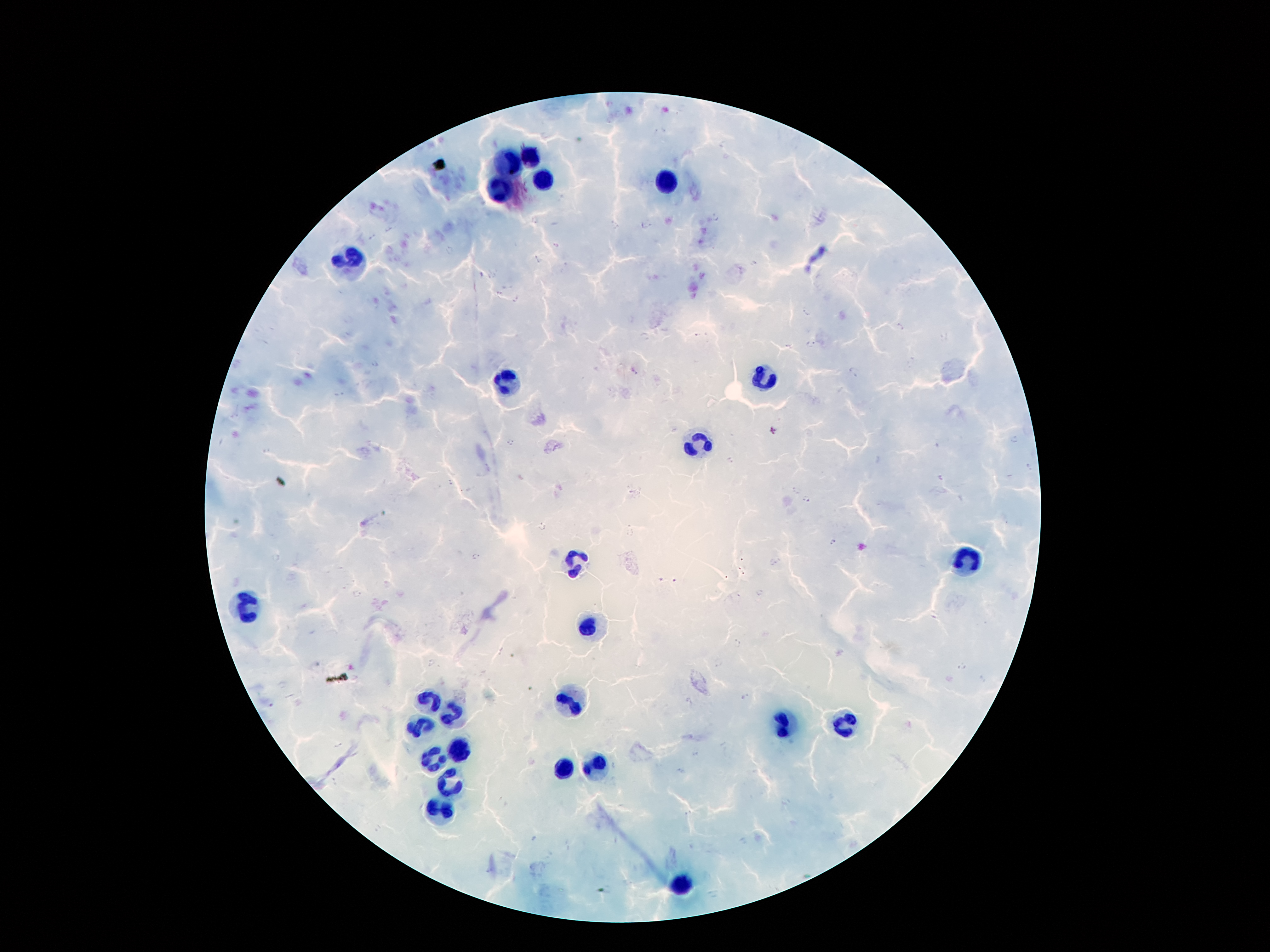

coordinate format = approximate centers as (x, y) in pixels
Plasmodium parasite locations = (714, 219), (645, 225), (389, 230), (371, 236), (537, 260), (499, 294), (515, 299), (806, 313), (899, 327), (697, 335), (810, 344), (788, 345), (375, 365), (633, 371), (853, 371), (338, 394), (235, 415), (1014, 439), (511, 442), (267, 452), (731, 460), (942, 477), (449, 483), (796, 489), (804, 500), (541, 527), (833, 541), (275, 557), (476, 557), (675, 581), (760, 593), (356, 594), (736, 645), (433, 664), (720, 664), (283, 685), (747, 697), (338, 745), (696, 752), (680, 771), (335, 782)
leukocyte locations = (528, 158), (511, 164), (542, 182), (668, 182), (500, 193), (354, 261), (758, 379), (508, 383), (696, 445), (966, 557), (572, 562), (248, 606), (586, 628), (573, 699), (429, 701), (449, 712), (842, 721), (782, 723), (422, 728), (458, 752), (433, 761), (592, 765), (564, 772), (453, 785), (438, 809), (681, 882)
patient malaria status = infected with Plasmodium falciparum
stain = Giemsa
magnification = 100x
field of view = single
image size = 1270×952 pixels
preparation = thick peripheral-blood smear
capture = smartphone camera through the microscope eyepiece